Locate and identify every blood parasite.
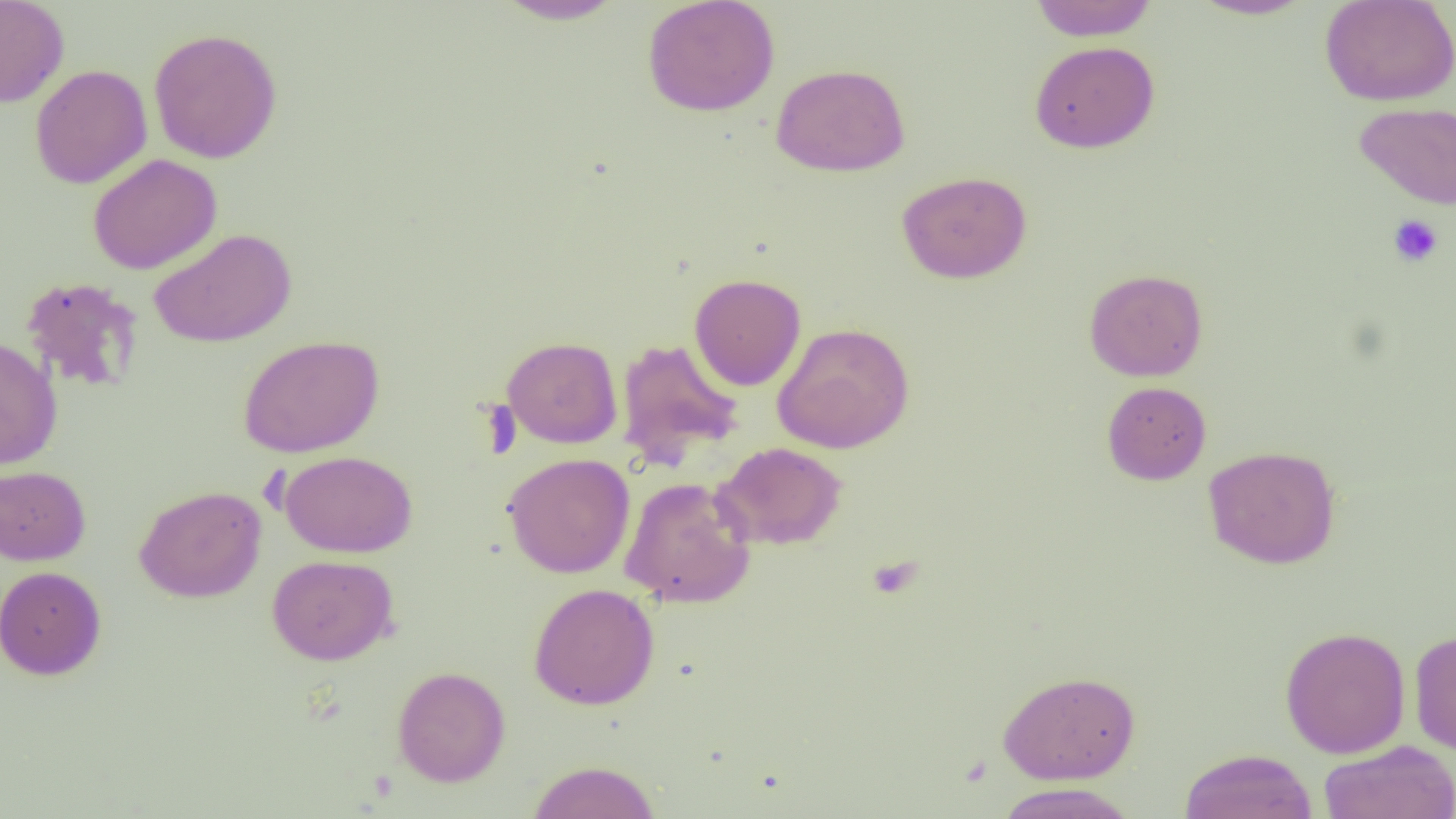
No blood parasites seen.

Approximate bounding boxes as (x1, y1, x2, y2) in pixels. Uninfected red blood cell locations: (0, 0, 69, 108), (493, 0, 627, 25), (642, 0, 780, 116), (1029, 0, 1158, 41), (1189, 0, 1316, 20), (1319, 0, 1456, 106), (149, 27, 282, 164), (1029, 40, 1159, 153), (771, 63, 910, 177), (30, 65, 152, 188), (1354, 101, 1455, 209), (88, 154, 222, 275), (896, 171, 1032, 284), (149, 228, 296, 348), (1084, 268, 1208, 381), (689, 273, 806, 390), (20, 276, 144, 394), (772, 322, 915, 453), (237, 335, 385, 458), (502, 336, 622, 449), (0, 337, 63, 470), (616, 338, 745, 466), (1102, 381, 1211, 484), (712, 441, 848, 550), (1203, 445, 1341, 569), (279, 450, 417, 558), (502, 452, 635, 578), (0, 464, 91, 566), (620, 476, 757, 608), (134, 485, 266, 603), (267, 554, 398, 665), (0, 565, 107, 681), (528, 583, 660, 710), (1280, 625, 1411, 758), (1409, 629, 1456, 756), (392, 666, 510, 787), (997, 669, 1140, 784), (1319, 740, 1456, 819), (1179, 748, 1318, 819), (525, 760, 661, 819), (994, 782, 1137, 819). Platelet locations: (1387, 214, 1443, 267), (867, 555, 922, 599). Slide-level diagnosis: no evidence of blood parasites. Optical microscopy. Thin blood smear. Image is 1456×819 pixels. One field of a larger specimen. Captured at 1000x magnification.